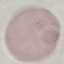

Summary:
  - Result: negative for malaria parasites
  - Stain: Giemsa
  - Image type: automatically extracted cell patch, resized to 64 × 64 pixels
  - Preparation: thin blood film
  - Capture: smartphone camera at the microscope eyepiece